Classify this cell by malaria status.
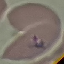
Parasitized.

Photographed with a smartphone camera at the microscope eyepiece. Automatically extracted cell patch, resized to 64 × 64 pixels. Giemsa stain. Thin smear of blood.